Locate every uninfected red blood cell.
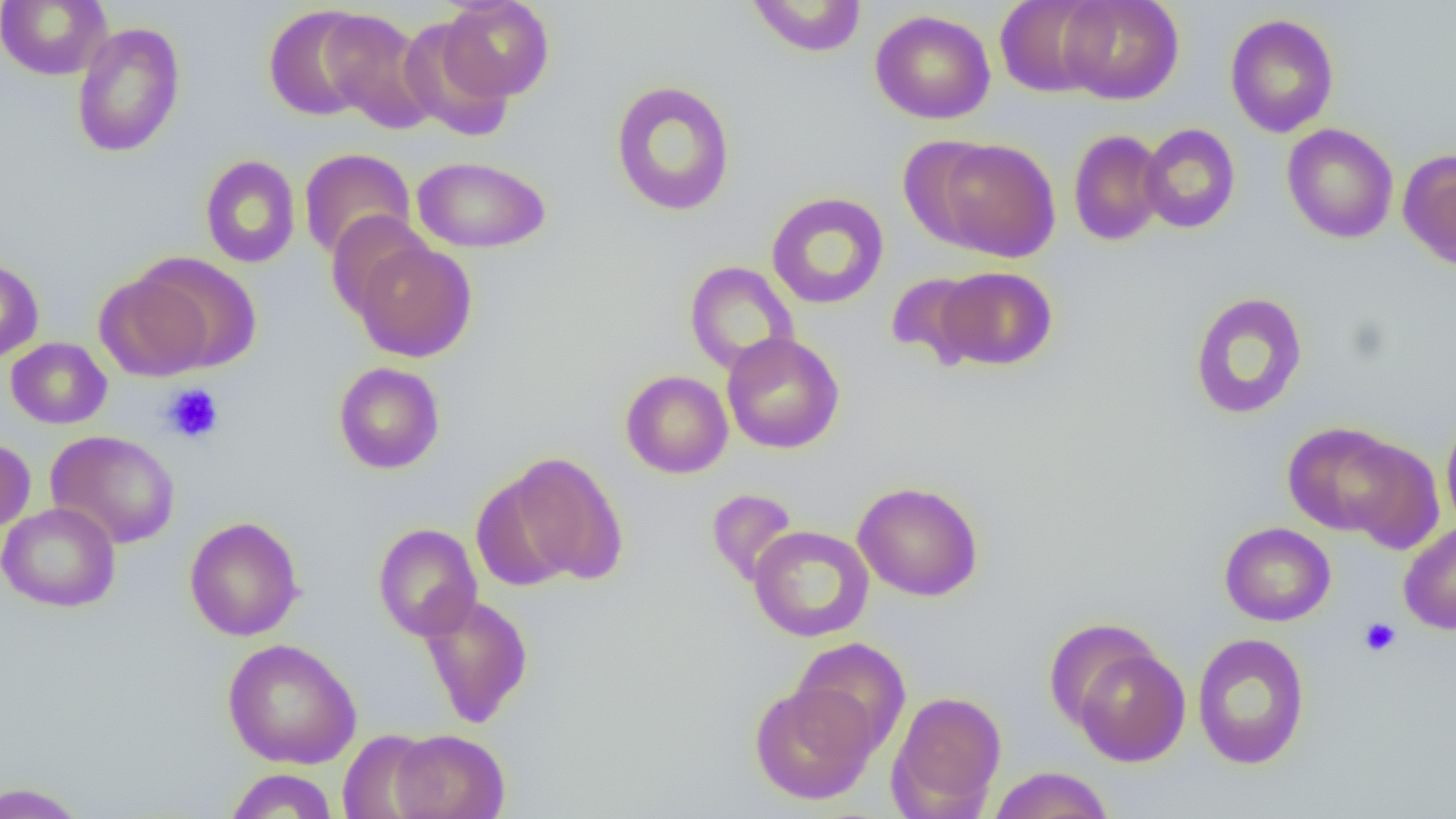

Approximate bounding boxes as [x1, y1, x2, y2] in pixels.
Uninfected red blood cells: [0, 0, 111, 80], [440, 0, 555, 102], [746, 0, 867, 57], [995, 0, 1110, 97], [1057, 0, 1185, 105], [263, 4, 378, 122], [319, 9, 438, 133], [870, 10, 995, 124], [1225, 13, 1339, 138], [399, 16, 515, 140], [70, 22, 186, 158], [610, 80, 736, 217], [1282, 123, 1398, 243], [1138, 124, 1240, 234], [1068, 129, 1167, 246], [931, 137, 1060, 262], [298, 148, 416, 261], [1398, 149, 1456, 270], [200, 155, 301, 268], [412, 156, 551, 253], [766, 192, 889, 309], [325, 212, 431, 320], [350, 238, 478, 362], [132, 253, 261, 373], [0, 258, 44, 363], [684, 261, 799, 375], [936, 266, 1057, 370], [95, 271, 213, 381], [886, 272, 988, 370], [1188, 291, 1308, 420], [721, 332, 845, 454], [6, 338, 112, 429], [333, 362, 445, 474], [621, 370, 733, 478], [1441, 411, 1456, 531], [1281, 421, 1416, 540], [45, 430, 181, 550], [1336, 433, 1444, 552], [0, 438, 35, 532], [500, 452, 629, 585], [853, 481, 984, 601], [706, 487, 800, 587], [0, 502, 120, 612], [185, 516, 304, 641], [1398, 521, 1456, 635], [1219, 522, 1335, 626], [372, 523, 483, 641], [749, 525, 874, 642], [420, 594, 534, 729], [1191, 632, 1310, 770], [790, 637, 911, 757], [223, 638, 362, 769], [1067, 641, 1191, 767], [748, 680, 879, 805], [888, 690, 1007, 817], [337, 729, 440, 819], [388, 729, 509, 819], [987, 766, 1114, 819], [224, 768, 339, 818], [0, 781, 89, 819].

slide-level diagnosis = negative for blood parasites
platelet locations = approximate bounding boxes as [x1, y1, x2, y2] in pixels: [162, 383, 224, 443], [1359, 617, 1401, 657]
field of view = single
modality = optical microscopy
image size = 1456×819 pixels
magnification = 1000x
preparation = thin blood smear